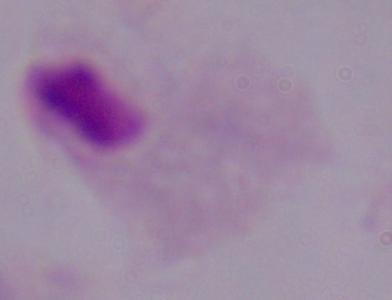
Summary:
  - Magnification: 1000x
  - Identification: trichomonad
  - Modality: photomicrograph